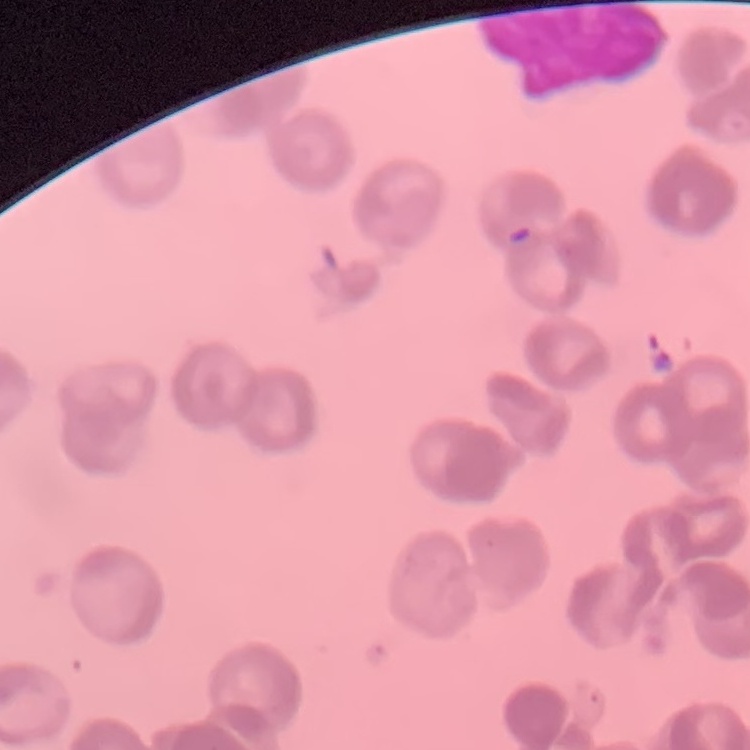
Summary:
  - Erythrocyte morphology: rouleaux formation
  - Stain: Field's or Giemsa
  - Image type: one tile cut from a larger photomicrograph
  - Preparation: thin blood smear